Name the cell type shown.
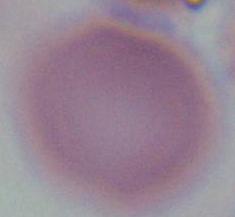
This is an erythrocyte.

{
  "modality": "micrograph",
  "magnification": "1000x"
}